Locate every uninfected red blood cell.
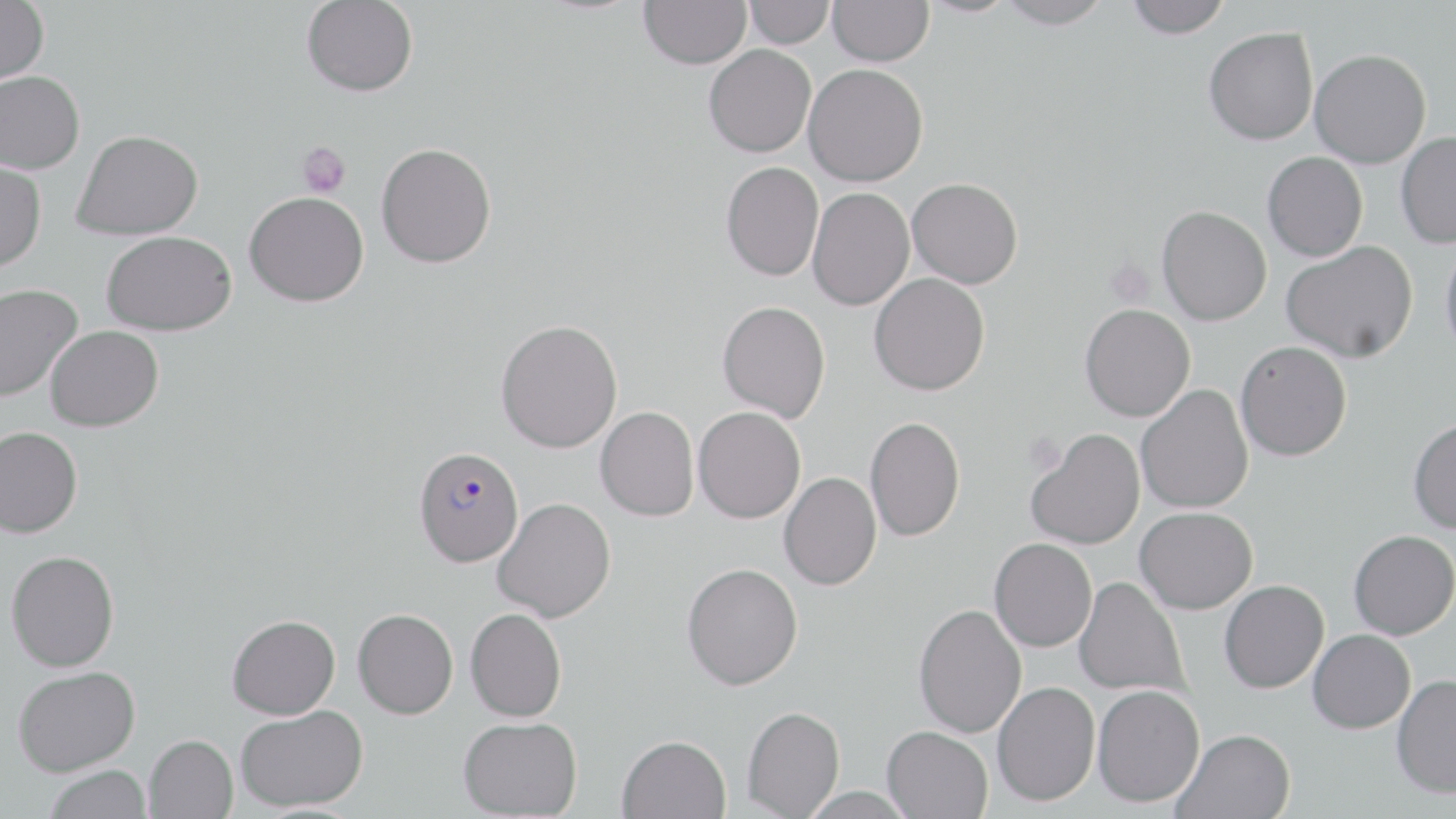

Approximate bounding boxes as (x1, y1, x2, y2) in pixels.
Uninfected red blood cells: (302, 0, 418, 97), (639, 0, 751, 69), (828, 0, 934, 66), (916, 0, 1021, 17), (996, 0, 1114, 29), (1125, 0, 1231, 38), (0, 1, 48, 86), (744, 1, 835, 48), (1204, 27, 1318, 145), (704, 44, 816, 157), (1310, 49, 1431, 168), (803, 63, 928, 187), (0, 71, 85, 174), (73, 129, 203, 240), (1396, 131, 1456, 248), (376, 142, 497, 268), (1262, 151, 1368, 261), (0, 159, 47, 273), (721, 161, 824, 281), (907, 177, 1023, 289), (807, 187, 915, 310), (244, 191, 369, 307), (1157, 205, 1272, 325), (102, 230, 237, 335), (1439, 238, 1456, 361), (1281, 240, 1418, 363), (869, 273, 990, 396), (0, 284, 81, 403), (717, 300, 830, 423), (1080, 304, 1195, 421), (495, 319, 622, 453), (45, 325, 163, 432), (1235, 340, 1352, 461), (1136, 384, 1254, 513), (595, 406, 699, 521), (693, 406, 806, 523), (864, 416, 966, 543), (1408, 418, 1456, 533), (0, 426, 83, 538), (1026, 428, 1145, 550), (778, 471, 882, 590), (492, 497, 615, 622), (1134, 507, 1257, 614), (1349, 529, 1456, 640), (989, 538, 1097, 652), (6, 550, 119, 672), (681, 563, 802, 690), (1073, 577, 1188, 698), (1219, 580, 1329, 693), (913, 604, 1027, 738), (353, 608, 458, 719), (466, 608, 567, 721), (227, 615, 340, 719), (1308, 629, 1416, 733), (13, 665, 140, 776), (1391, 674, 1456, 799), (992, 681, 1100, 806), (1092, 684, 1205, 807), (235, 705, 367, 811), (742, 706, 845, 818), (458, 717, 582, 819), (882, 725, 993, 819), (1173, 728, 1296, 819), (143, 734, 237, 819), (617, 734, 731, 819), (43, 764, 153, 819).

Plasmodium falciparum-infected red blood cell locations: (413, 446, 524, 567). Platelet locations: (297, 142, 351, 198), (1024, 431, 1067, 476). Slide-level diagnosis: Plasmodium falciparum. Single field of view. Image is 1456×819 pixels. Optical microscopy. May-Grünwald-Giemsa stain. Thin blood film. 1000x magnification.